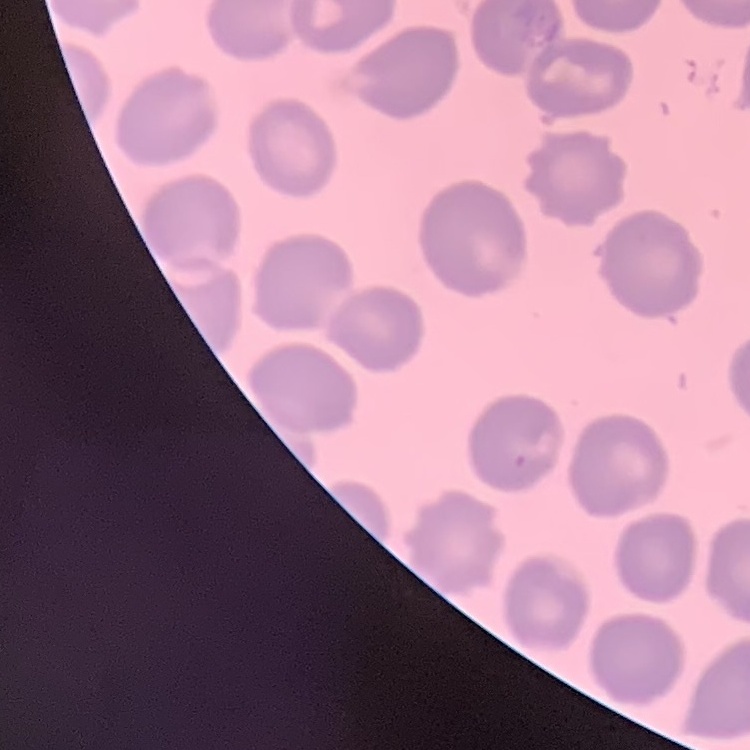
red blood cell morphology = no rouleaux formation
preparation = thin blood film
image type = square crop of a larger photomicrograph
stain = Field's or Giemsa